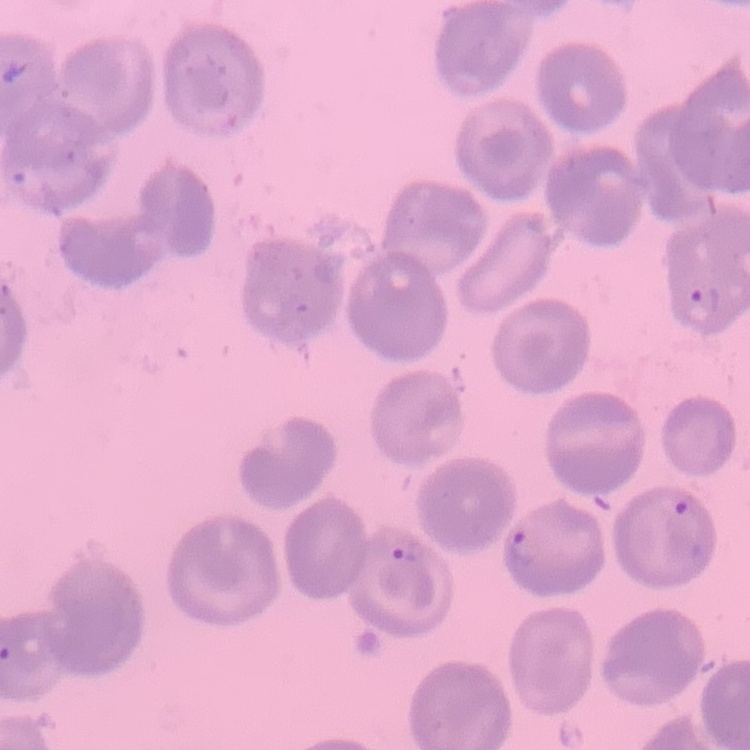
erythrocyte_morphology: no rouleaux formation
image_type: square crop of a larger photomicrograph
preparation: thin blood film
stain: Field's or Giemsa